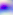 Toxoplasma gondii is seen. Micrograph. Captured at 400x magnification.